Report the malaria status of this cell.
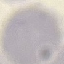

Uninfected.

Photographed with a smartphone camera at the microscope eyepiece. Giemsa stain. Cell patch, automatically extracted from a larger field of view and resized to 64 × 64 pixels. Thin blood smear.